Comment on the morphology of the erythrocytes.
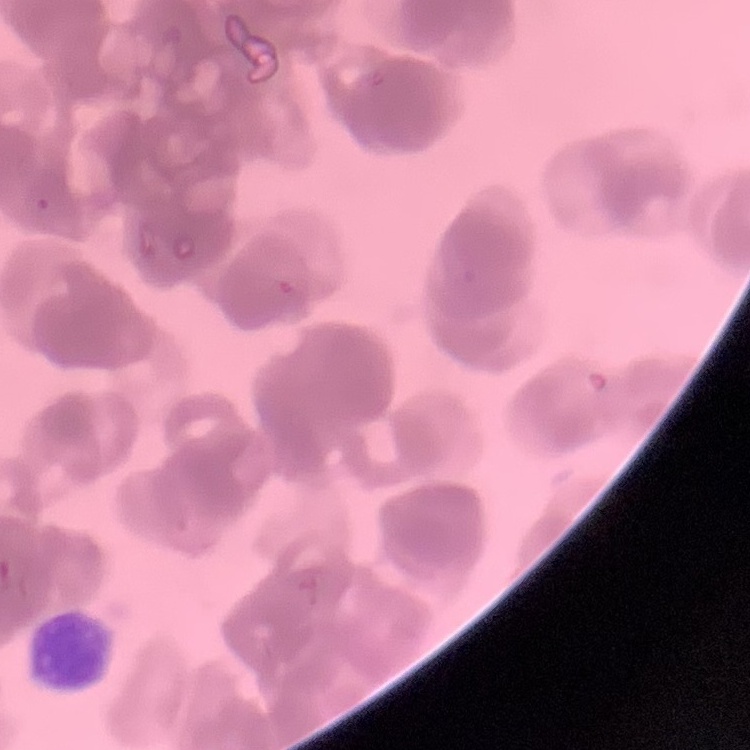

Rouleaux formation.

Square crop of a larger photomicrograph. Field's or Giemsa stain. Thin blood film.